Locate every blood parasite and identify its species.
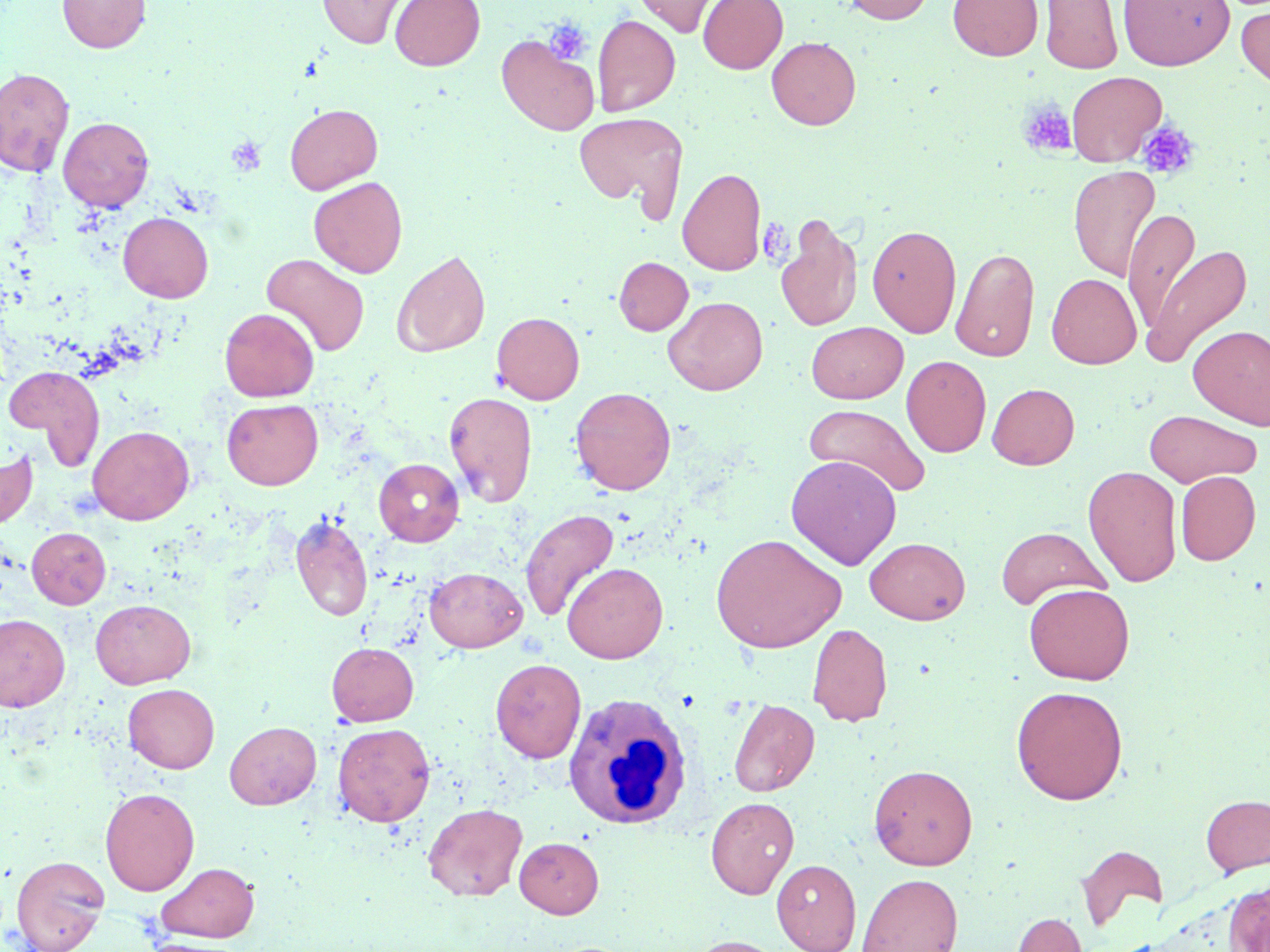
No blood parasites seen.

slide-level diagnosis = negative for blood parasites
stain = May-Grünwald-Giemsa
field of view = one of a larger specimen
uninfected red blood cell locations = approximate bounding boxes as [x1, y1, x2, y2] in pixels: [58, 0, 150, 53], [317, 0, 414, 49], [390, 0, 485, 70], [629, 0, 727, 37], [698, 0, 788, 73], [841, 0, 935, 24], [948, 0, 1043, 60], [1118, 0, 1235, 70], [1040, 1, 1123, 74], [1236, 4, 1270, 92], [593, 14, 680, 116], [497, 34, 600, 135], [766, 36, 861, 129], [0, 67, 75, 177], [1066, 71, 1165, 166], [285, 103, 382, 194], [574, 111, 688, 217], [58, 116, 154, 212], [1068, 165, 1160, 282], [678, 167, 766, 276], [308, 176, 408, 277], [1123, 209, 1201, 331], [118, 212, 213, 303], [776, 215, 863, 333], [867, 224, 962, 338], [1141, 244, 1250, 368], [951, 247, 1039, 361], [391, 249, 491, 357], [261, 253, 369, 357], [614, 257, 693, 335], [1047, 274, 1141, 368], [663, 296, 768, 395], [219, 307, 319, 401], [492, 312, 584, 404], [806, 321, 908, 404], [1188, 325, 1270, 429], [901, 355, 991, 457], [6, 365, 105, 468], [987, 383, 1080, 469], [570, 387, 676, 495], [444, 390, 538, 508], [222, 399, 323, 489], [804, 404, 931, 498], [1144, 410, 1261, 487], [88, 425, 194, 524], [0, 449, 38, 530], [786, 455, 902, 569], [373, 458, 463, 546], [1083, 465, 1182, 587], [1176, 471, 1260, 565], [520, 508, 619, 623], [290, 514, 373, 622], [996, 526, 1109, 610], [27, 527, 111, 609], [710, 533, 846, 653], [865, 537, 970, 624], [562, 562, 668, 663], [424, 567, 527, 652], [1024, 583, 1134, 684], [90, 599, 196, 689], [0, 614, 70, 711], [807, 622, 893, 727], [327, 642, 418, 726], [490, 658, 586, 763], [123, 684, 219, 773], [1011, 685, 1128, 804], [728, 698, 819, 796], [224, 721, 321, 809], [332, 722, 435, 826], [868, 763, 978, 870], [100, 787, 200, 895], [1201, 794, 1270, 875], [706, 797, 799, 899], [423, 802, 527, 901], [514, 837, 604, 918], [1076, 844, 1168, 930], [10, 854, 110, 952], [771, 859, 861, 952], [157, 862, 259, 942], [857, 872, 963, 952], [1224, 881, 1270, 950], [1012, 912, 1087, 952], [681, 935, 791, 952], [138, 937, 249, 952]
image size = 1270×952 pixels
modality = light microscopy
magnification = 1000x
white blood cell locations = approximate bounding boxes as [x1, y1, x2, y2] in pixels: [562, 691, 693, 830]
platelet locations = approximate bounding boxes as [x1, y1, x2, y2] in pixels: [544, 18, 592, 65], [1018, 100, 1077, 158], [1137, 121, 1199, 180], [226, 136, 266, 177]
preparation = thin blood smear